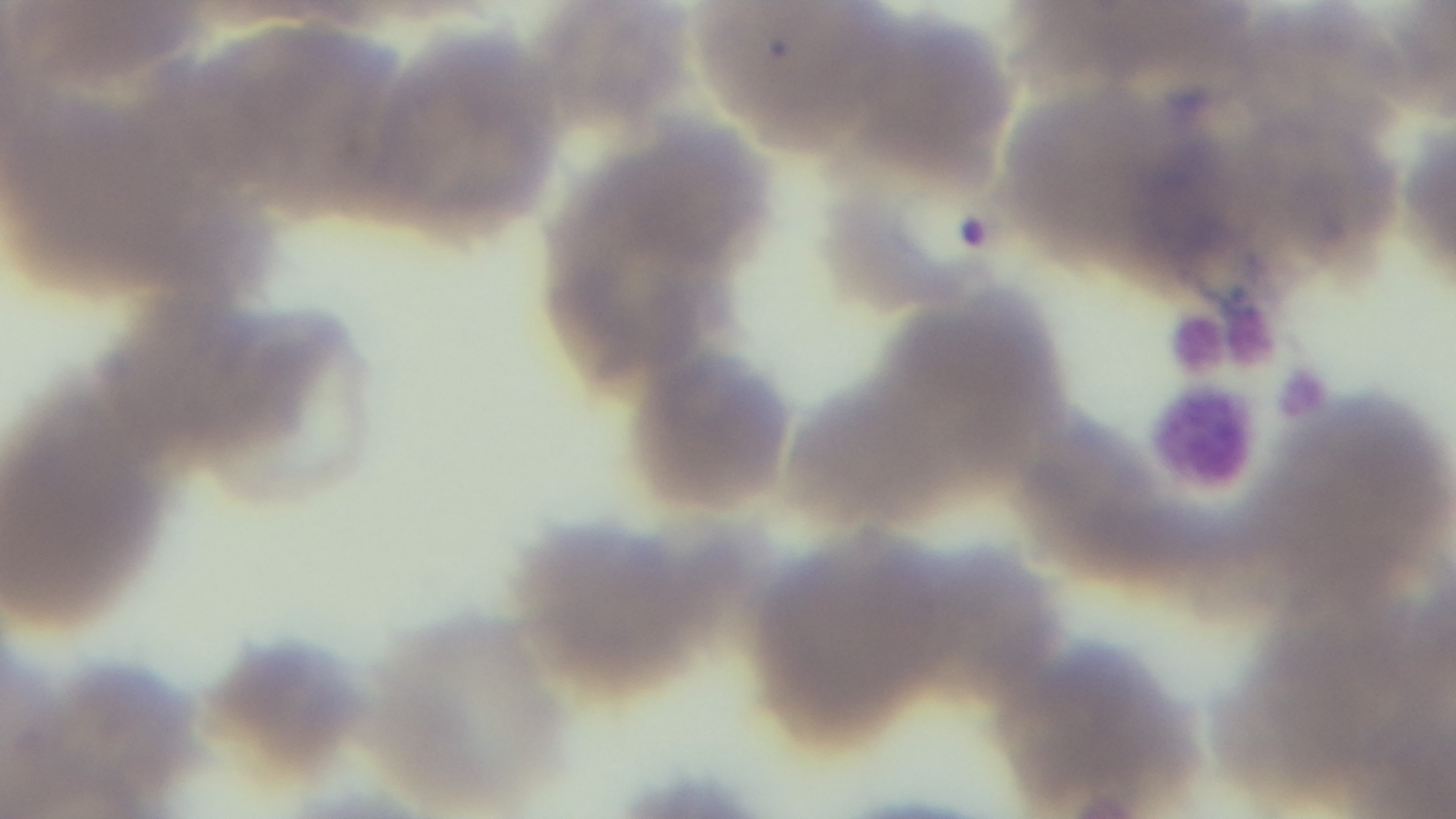

modality = light microscopy
stain = Giemsa
preparation = thin
malaria status = positive
objective = 100x oil immersion
capture = mounted 4K digital camera
field of view = single